Classify this cell by malaria status.
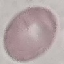

Uninfected.

Photographed with a smartphone camera at the microscope eyepiece. Automatically extracted cell patch, resized to 64 × 64 pixels. Thin smear of blood. Giemsa stain.